Name the blood parasite species.
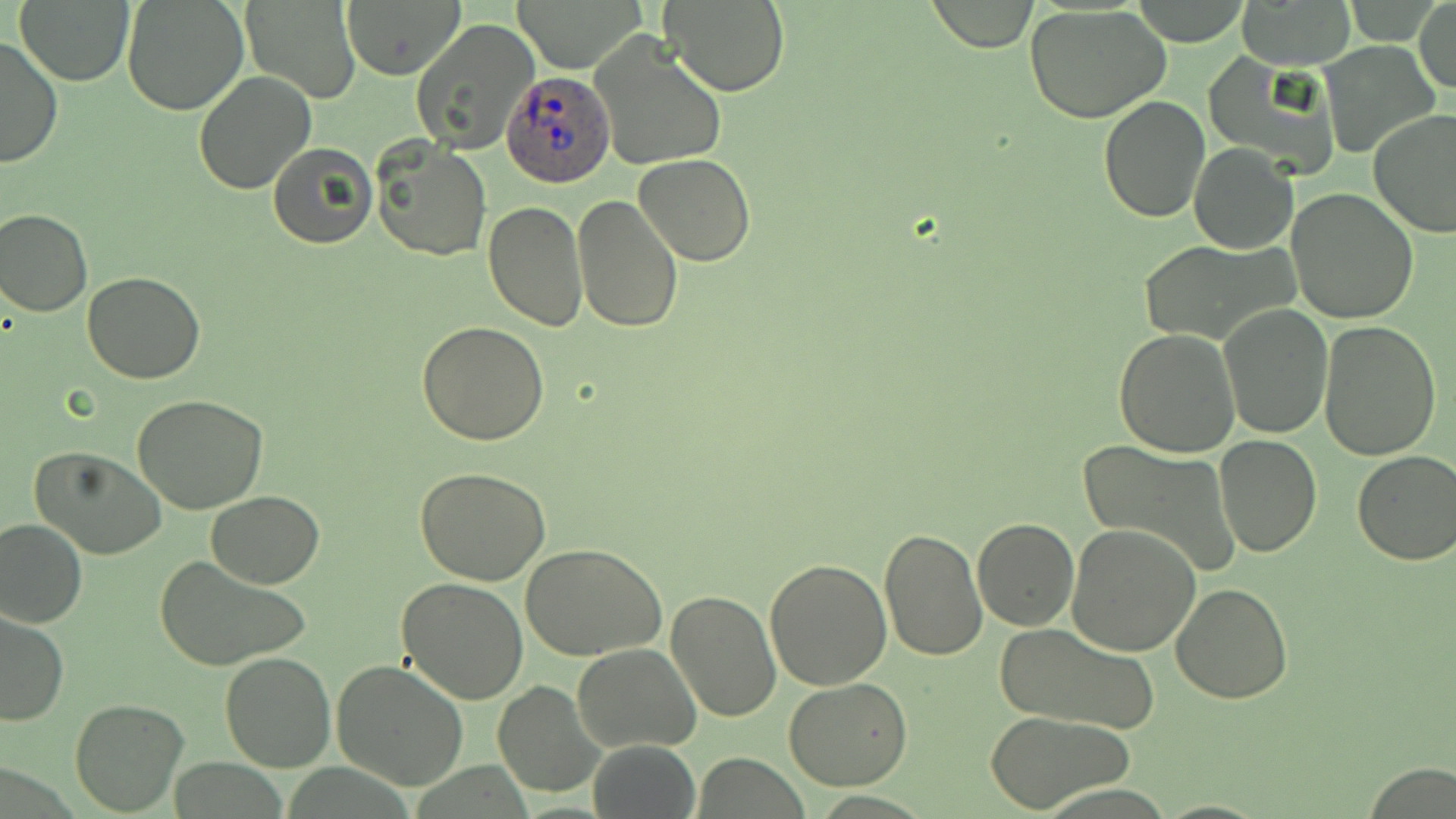

Plasmodium ovale.

Summary:
  - Coordinate format: approximate bounding boxes as named x1/y1/x2/y2 corners in pixels
  - Plasmodium ovale-infected red blood cell locations: (x1=504, y1=70, x2=614, y2=187)
  - Uninfected red blood cell locations: (x1=16, y1=0, x2=135, y2=87), (x1=121, y1=0, x2=250, y2=116), (x1=340, y1=0, x2=466, y2=79), (x1=510, y1=0, x2=645, y2=71), (x1=662, y1=0, x2=788, y2=97), (x1=242, y1=1, x2=362, y2=102), (x1=927, y1=1, x2=1038, y2=52), (x1=1413, y1=1, x2=1455, y2=95), (x1=1128, y1=2, x2=1253, y2=44), (x1=1234, y1=2, x2=1354, y2=68), (x1=1024, y1=5, x2=1169, y2=122), (x1=409, y1=19, x2=540, y2=157), (x1=589, y1=33, x2=727, y2=173), (x1=0, y1=36, x2=65, y2=171), (x1=1320, y1=43, x2=1440, y2=159), (x1=1207, y1=54, x2=1341, y2=178), (x1=192, y1=71, x2=317, y2=194), (x1=1098, y1=96, x2=1211, y2=224), (x1=1369, y1=109, x2=1456, y2=239), (x1=372, y1=140, x2=492, y2=263), (x1=267, y1=143, x2=377, y2=250), (x1=1189, y1=143, x2=1298, y2=254), (x1=634, y1=154, x2=755, y2=267), (x1=1287, y1=187, x2=1420, y2=323), (x1=572, y1=192, x2=682, y2=332), (x1=483, y1=201, x2=588, y2=333), (x1=0, y1=208, x2=93, y2=317), (x1=1136, y1=238, x2=1292, y2=343), (x1=82, y1=273, x2=206, y2=384), (x1=1218, y1=304, x2=1332, y2=439), (x1=1318, y1=319, x2=1441, y2=461), (x1=417, y1=322, x2=550, y2=444), (x1=1114, y1=329, x2=1241, y2=458), (x1=134, y1=394, x2=269, y2=514), (x1=1214, y1=435, x2=1322, y2=556), (x1=1077, y1=440, x2=1243, y2=580), (x1=30, y1=447, x2=167, y2=560), (x1=1352, y1=451, x2=1456, y2=567), (x1=414, y1=467, x2=552, y2=586), (x1=207, y1=492, x2=325, y2=588), (x1=0, y1=517, x2=88, y2=630), (x1=972, y1=518, x2=1078, y2=632), (x1=1065, y1=521, x2=1201, y2=657), (x1=878, y1=528, x2=987, y2=662), (x1=522, y1=544, x2=666, y2=661), (x1=765, y1=556, x2=893, y2=690), (x1=156, y1=557, x2=313, y2=670), (x1=396, y1=576, x2=529, y2=704), (x1=1171, y1=581, x2=1293, y2=702), (x1=664, y1=588, x2=781, y2=723), (x1=0, y1=610, x2=70, y2=727), (x1=993, y1=623, x2=1159, y2=736), (x1=572, y1=644, x2=700, y2=752), (x1=219, y1=652, x2=337, y2=772), (x1=332, y1=660, x2=469, y2=790), (x1=783, y1=677, x2=914, y2=789), (x1=492, y1=681, x2=604, y2=799), (x1=70, y1=699, x2=187, y2=815), (x1=985, y1=710, x2=1134, y2=812), (x1=588, y1=741, x2=699, y2=819), (x1=1364, y1=763, x2=1453, y2=818)
  - Stain: May-Grünwald-Giemsa
  - Field of view: single
  - Magnification: 1000x
  - Image size: 1456×819 pixels
  - Preparation: thin blood smear
  - Modality: light microscopy